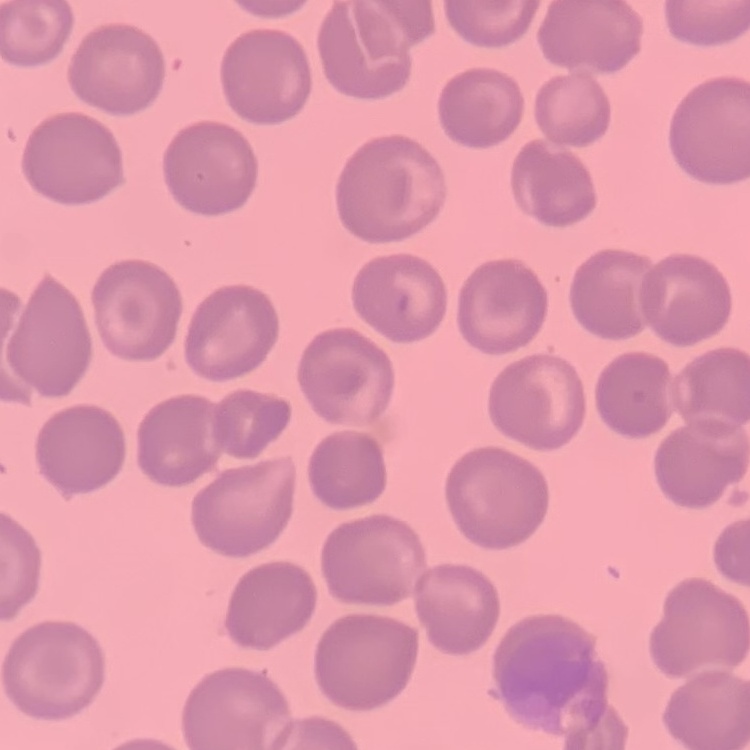
red_blood_cell_morphology: no rouleaux formation
image_type: square crop of a larger photomicrograph
stain: Field's or Giemsa
preparation: thin blood smear